Assess for malaria.
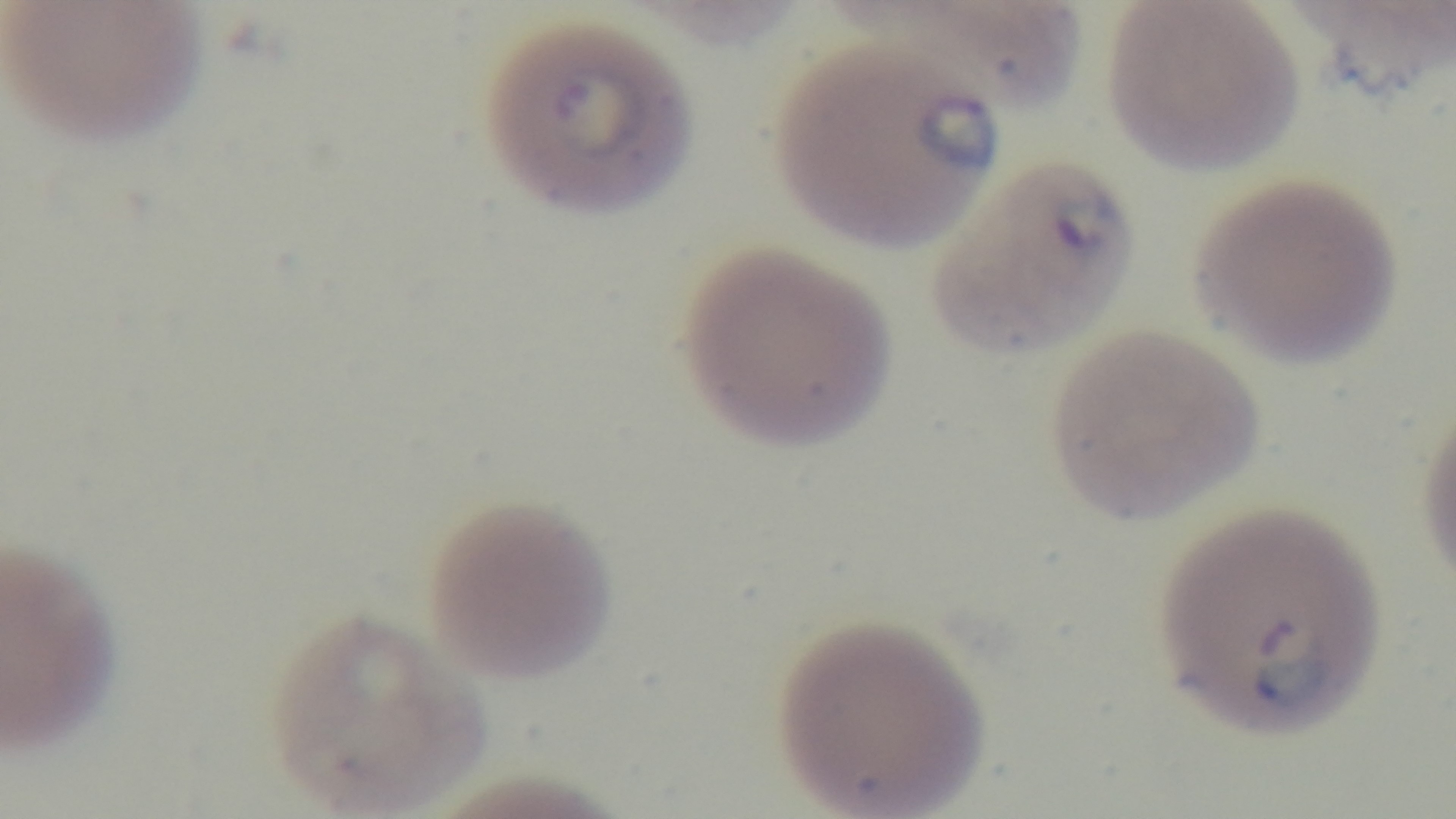

Positive.

100x oil-immersion objective. Photomicrograph. Mounted 4K digital camera. Giemsa stain. Single field of view. Preparation: thin smear.